State the blood parasite species.
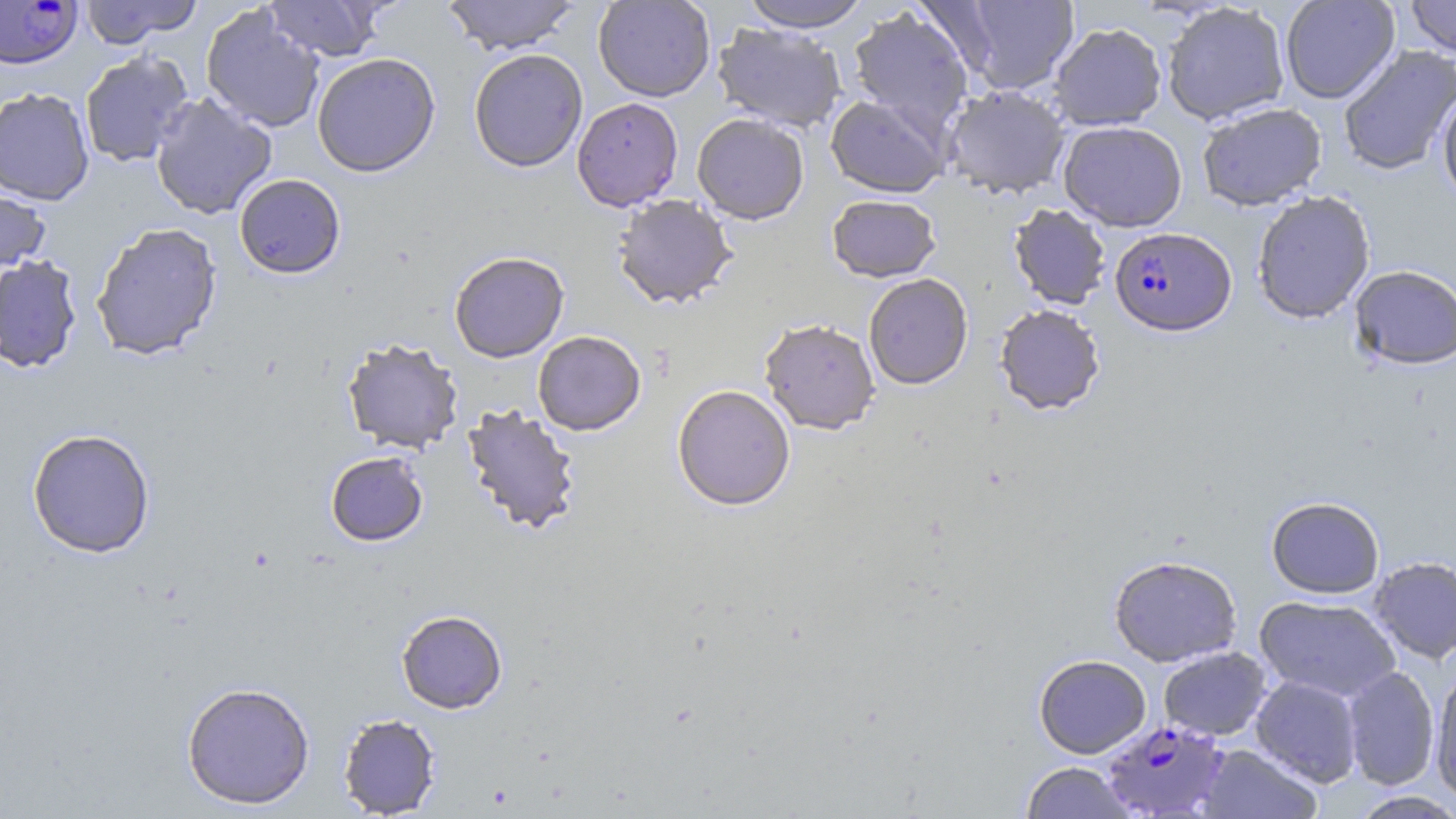

Plasmodium falciparum.

Approximate bounding boxes as [x1, y1, x2, y2] in pixels. Plasmodium falciparum-infected red blood cell locations: [0, 0, 83, 69], [1110, 227, 1236, 337], [1102, 719, 1229, 818]. Uninfected red blood cell locations: [80, 0, 202, 47], [263, 0, 386, 62], [442, 0, 580, 55], [593, 0, 715, 102], [736, 0, 873, 32], [949, 0, 1079, 95], [1280, 0, 1400, 104], [1405, 0, 1456, 59], [1161, 3, 1291, 125], [201, 5, 325, 133], [847, 7, 974, 138], [712, 23, 847, 133], [1048, 23, 1167, 131], [1338, 45, 1456, 176], [469, 48, 588, 172], [79, 51, 194, 168], [311, 52, 440, 177], [942, 85, 1070, 199], [1437, 85, 1456, 207], [0, 87, 95, 205], [150, 92, 277, 220], [825, 94, 951, 198], [572, 97, 683, 211], [1197, 102, 1327, 211], [692, 113, 810, 225], [1058, 121, 1188, 232], [234, 174, 346, 278], [0, 184, 51, 276], [1252, 190, 1375, 324], [827, 194, 941, 283], [612, 195, 738, 310], [1009, 204, 1111, 309], [90, 222, 223, 361], [449, 251, 569, 363], [0, 254, 83, 373], [1349, 265, 1456, 371], [863, 273, 973, 390], [994, 304, 1105, 415], [759, 318, 880, 435], [533, 330, 646, 435], [342, 337, 464, 454], [672, 384, 796, 512], [461, 404, 582, 536], [26, 427, 156, 558], [325, 452, 428, 546], [1266, 496, 1385, 599], [1109, 555, 1242, 667], [1368, 556, 1456, 663], [1254, 595, 1401, 702], [396, 610, 507, 713], [1158, 647, 1272, 741], [1034, 654, 1151, 758], [1342, 666, 1439, 790], [1429, 670, 1456, 802], [1250, 675, 1363, 787], [181, 681, 315, 809], [337, 712, 442, 817], [1197, 744, 1322, 818], [1020, 762, 1136, 818], [1350, 791, 1456, 818]. Single field of view. Thin blood film. Light microscopy. May-Grünwald-Giemsa-stained preparation. Captured at 1000x magnification. Image is 1456×819 pixels.